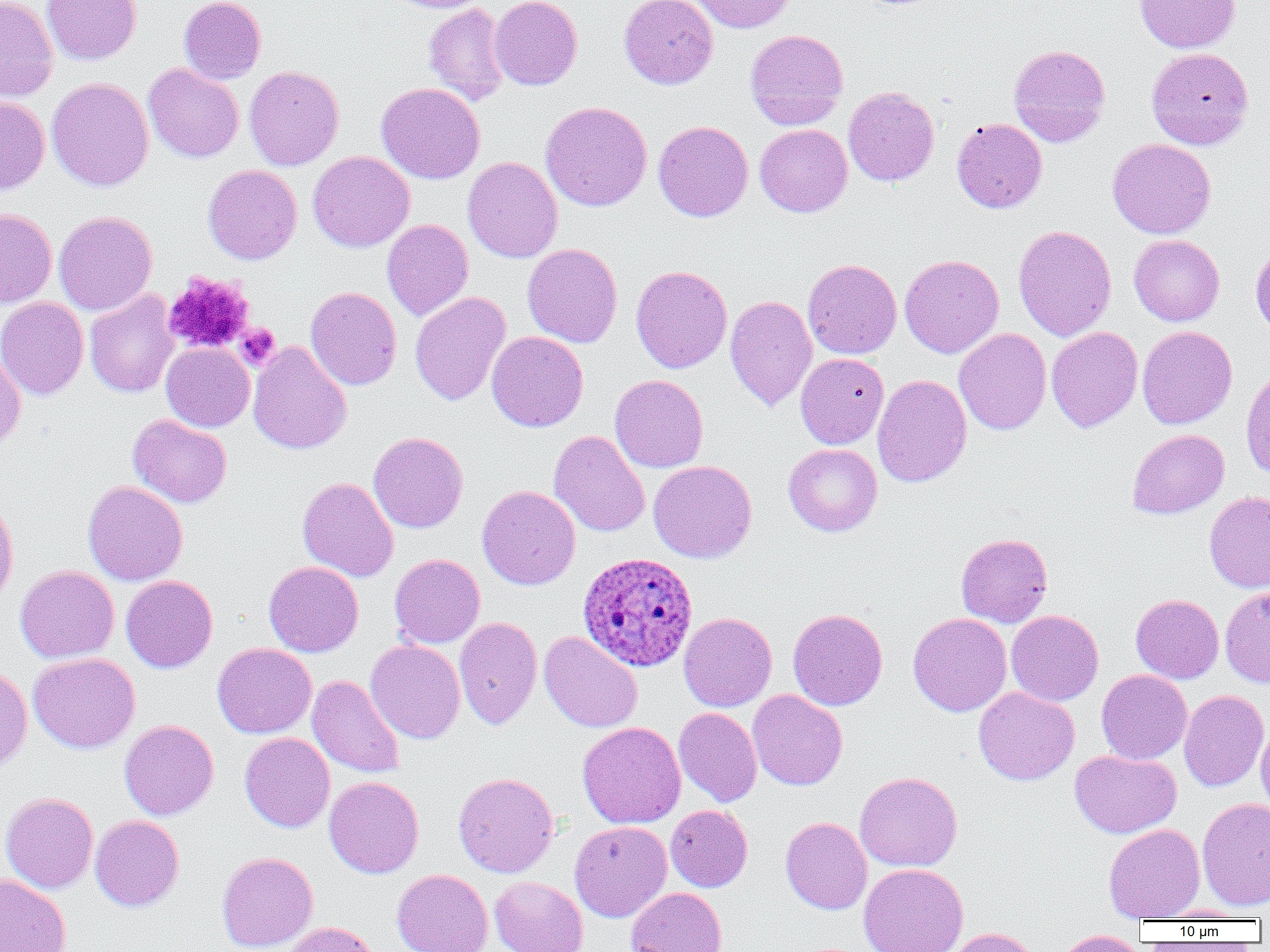
Summary:
  - Coordinate format: approximate bounding boxes as named x1/y1/x2/y2 corners in pixels
  - Plasmodium ovale-infected red blood cell locations: (x1=578, y1=551, x2=698, y2=672)
  - Platelet locations: (x1=163, y1=271, x2=255, y2=355), (x1=236, y1=323, x2=281, y2=370)
  - Uninfected red blood cell locations: (x1=0, y1=0, x2=58, y2=102), (x1=41, y1=0, x2=141, y2=65), (x1=178, y1=0, x2=266, y2=84), (x1=388, y1=0, x2=492, y2=13), (x1=489, y1=0, x2=582, y2=90), (x1=619, y1=0, x2=718, y2=90), (x1=690, y1=0, x2=796, y2=33), (x1=1135, y1=0, x2=1240, y2=53), (x1=423, y1=2, x2=512, y2=106), (x1=745, y1=29, x2=848, y2=130), (x1=1008, y1=44, x2=1111, y2=147), (x1=1146, y1=47, x2=1254, y2=150), (x1=142, y1=63, x2=244, y2=163), (x1=244, y1=66, x2=344, y2=171), (x1=46, y1=78, x2=154, y2=192), (x1=376, y1=82, x2=485, y2=184), (x1=843, y1=86, x2=939, y2=186), (x1=0, y1=96, x2=50, y2=194), (x1=540, y1=101, x2=652, y2=212), (x1=951, y1=118, x2=1047, y2=213), (x1=653, y1=120, x2=753, y2=222), (x1=755, y1=124, x2=853, y2=217), (x1=1107, y1=138, x2=1216, y2=239), (x1=307, y1=151, x2=415, y2=252), (x1=462, y1=156, x2=563, y2=263), (x1=202, y1=164, x2=302, y2=265), (x1=0, y1=209, x2=57, y2=308), (x1=53, y1=211, x2=157, y2=315), (x1=382, y1=219, x2=473, y2=321), (x1=1013, y1=225, x2=1117, y2=341), (x1=1129, y1=234, x2=1225, y2=326), (x1=522, y1=243, x2=622, y2=347), (x1=1251, y1=243, x2=1270, y2=341), (x1=899, y1=254, x2=1004, y2=358), (x1=802, y1=258, x2=901, y2=360), (x1=630, y1=265, x2=732, y2=373), (x1=305, y1=286, x2=402, y2=390), (x1=84, y1=288, x2=180, y2=398), (x1=410, y1=291, x2=511, y2=407), (x1=725, y1=295, x2=817, y2=411), (x1=0, y1=297, x2=89, y2=401), (x1=1137, y1=326, x2=1237, y2=429), (x1=1046, y1=327, x2=1143, y2=432), (x1=954, y1=328, x2=1051, y2=436), (x1=486, y1=331, x2=588, y2=432), (x1=248, y1=341, x2=351, y2=455), (x1=161, y1=342, x2=255, y2=432), (x1=0, y1=349, x2=26, y2=451), (x1=795, y1=352, x2=889, y2=449), (x1=1241, y1=368, x2=1270, y2=480), (x1=610, y1=374, x2=708, y2=473), (x1=872, y1=374, x2=972, y2=487), (x1=127, y1=414, x2=233, y2=508), (x1=1127, y1=429, x2=1229, y2=519), (x1=549, y1=430, x2=650, y2=537), (x1=368, y1=432, x2=468, y2=533), (x1=783, y1=443, x2=882, y2=536), (x1=648, y1=460, x2=757, y2=564), (x1=297, y1=477, x2=399, y2=582), (x1=83, y1=480, x2=188, y2=586), (x1=477, y1=485, x2=581, y2=590), (x1=1204, y1=491, x2=1270, y2=593), (x1=0, y1=498, x2=18, y2=610), (x1=956, y1=533, x2=1052, y2=627), (x1=389, y1=554, x2=485, y2=648), (x1=264, y1=561, x2=363, y2=657), (x1=14, y1=565, x2=119, y2=663), (x1=121, y1=575, x2=218, y2=673), (x1=1220, y1=586, x2=1270, y2=688), (x1=1130, y1=594, x2=1224, y2=683), (x1=788, y1=608, x2=887, y2=710), (x1=1006, y1=610, x2=1103, y2=706), (x1=678, y1=612, x2=777, y2=712), (x1=908, y1=612, x2=1011, y2=717), (x1=454, y1=617, x2=543, y2=729), (x1=539, y1=631, x2=642, y2=732), (x1=365, y1=640, x2=465, y2=743), (x1=212, y1=643, x2=316, y2=738), (x1=28, y1=652, x2=140, y2=754), (x1=0, y1=664, x2=32, y2=771), (x1=1096, y1=669, x2=1192, y2=764), (x1=306, y1=674, x2=406, y2=779), (x1=973, y1=687, x2=1080, y2=786), (x1=747, y1=689, x2=848, y2=790), (x1=1179, y1=690, x2=1269, y2=791), (x1=673, y1=707, x2=762, y2=807), (x1=119, y1=719, x2=219, y2=820), (x1=577, y1=722, x2=686, y2=828), (x1=1256, y1=723, x2=1270, y2=816), (x1=239, y1=732, x2=335, y2=832), (x1=1070, y1=749, x2=1181, y2=838), (x1=854, y1=771, x2=962, y2=872), (x1=453, y1=772, x2=559, y2=878), (x1=324, y1=776, x2=424, y2=878), (x1=0, y1=792, x2=98, y2=893), (x1=1197, y1=798, x2=1269, y2=911), (x1=665, y1=805, x2=752, y2=892), (x1=90, y1=815, x2=184, y2=912), (x1=780, y1=817, x2=872, y2=914), (x1=570, y1=821, x2=673, y2=922), (x1=1103, y1=823, x2=1205, y2=921), (x1=216, y1=852, x2=318, y2=952), (x1=858, y1=863, x2=969, y2=952), (x1=392, y1=869, x2=493, y2=951), (x1=1, y1=874, x2=71, y2=952), (x1=490, y1=876, x2=588, y2=952), (x1=626, y1=887, x2=728, y2=952), (x1=1152, y1=905, x2=1255, y2=921), (x1=283, y1=921, x2=381, y2=952), (x1=944, y1=927, x2=1041, y2=952), (x1=1053, y1=930, x2=1147, y2=952)
  - Slide-level diagnosis: Plasmodium ovale
  - Modality: light microscopy
  - Image size: 1270×952 pixels
  - Preparation: thin blood smear
  - Magnification: 1000x
  - Field of view: single